Comment on the morphology of the erythrocytes.
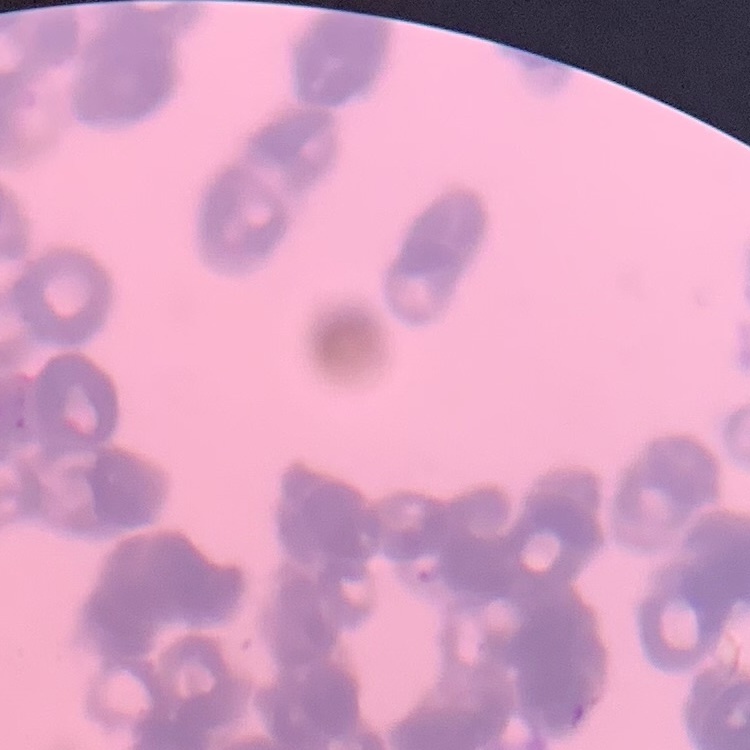
Rouleaux formation.

Summary:
  - Stain: Field's or Giemsa
  - Image type: one tile cut from a larger photomicrograph
  - Preparation: thin blood film